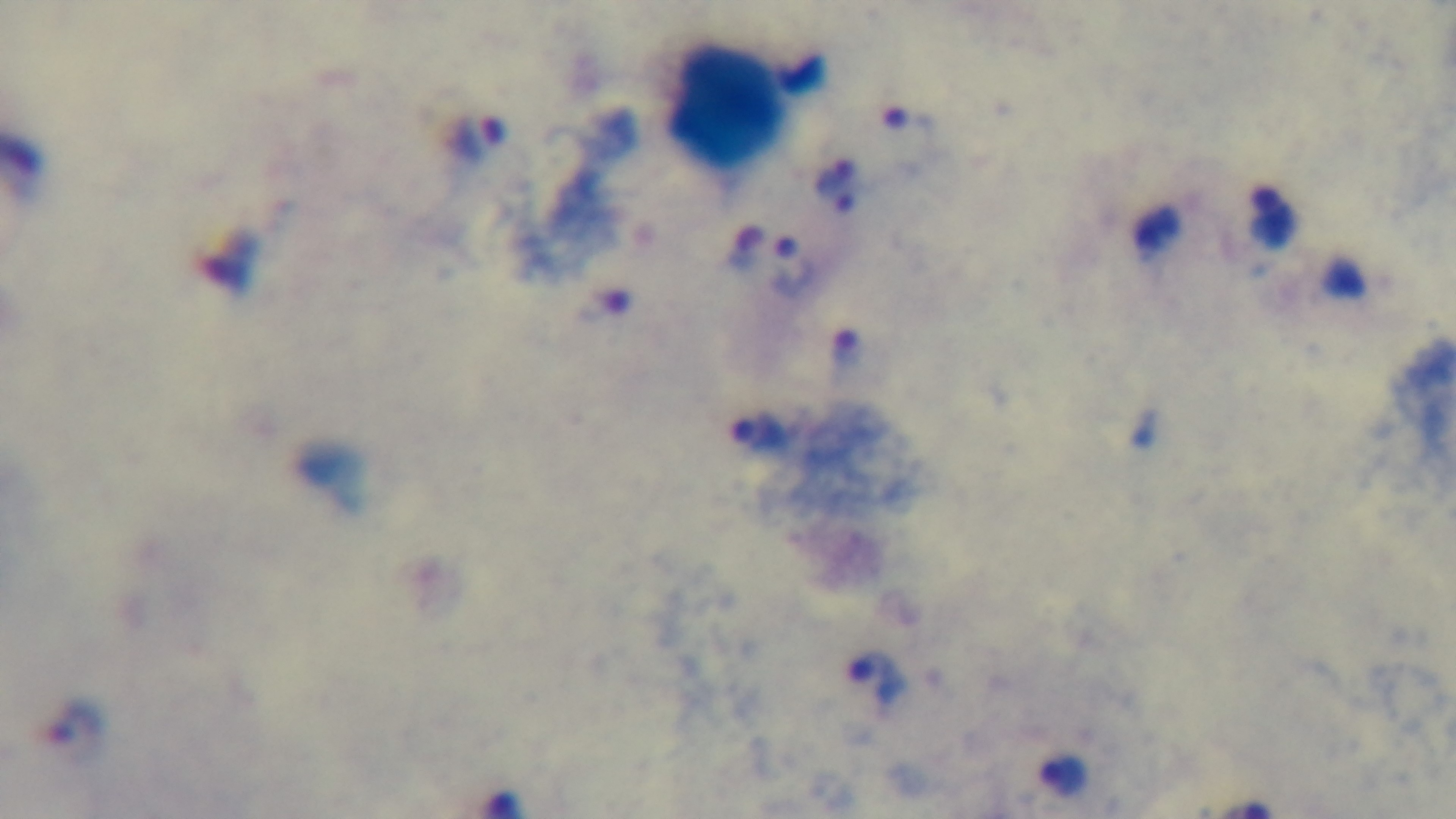

Summary:
  - Field of view: single
  - Preparation: thick smear
  - Stain: Giemsa
  - Capture: mounted 4K digital camera
  - Modality: light microscopy
  - Objective: 100x oil immersion
  - Malaria status: positive